Assess this cell for malaria.
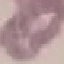

It is uninfected.

capture: smartphone camera at the microscope eyepiece
image_type: automatically extracted cell patch, resized to 64 × 64 pixels
stain: Giemsa
preparation: thin blood smear